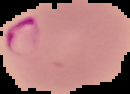 Segmented cell region on a black background. Image is 130×94 pixels. Result: malaria parasites detected. From a thin blood smear.